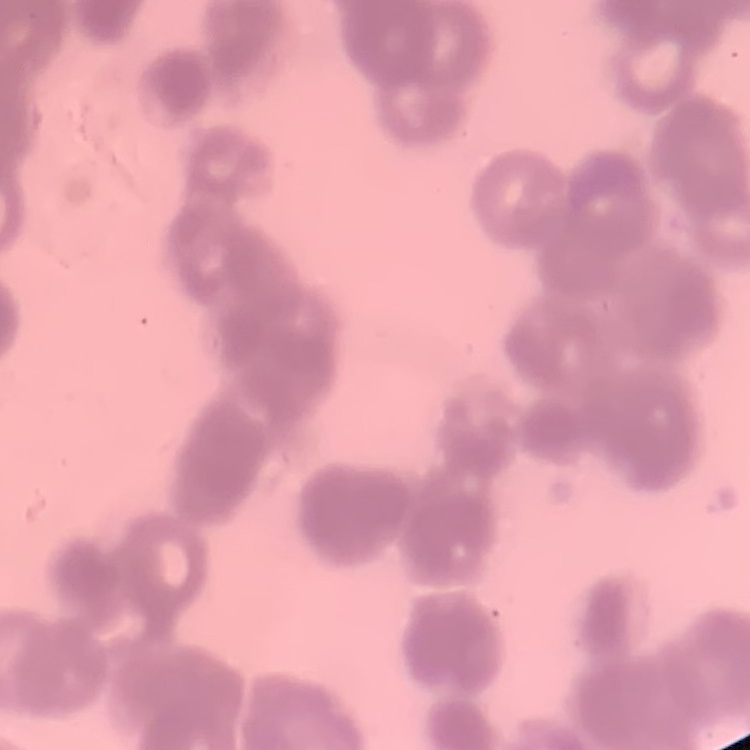
Summary:
  - Erythrocyte morphology: rouleaux formation
  - Stain: Field's or Giemsa
  - Image type: square crop of a larger photomicrograph
  - Preparation: thin blood smear